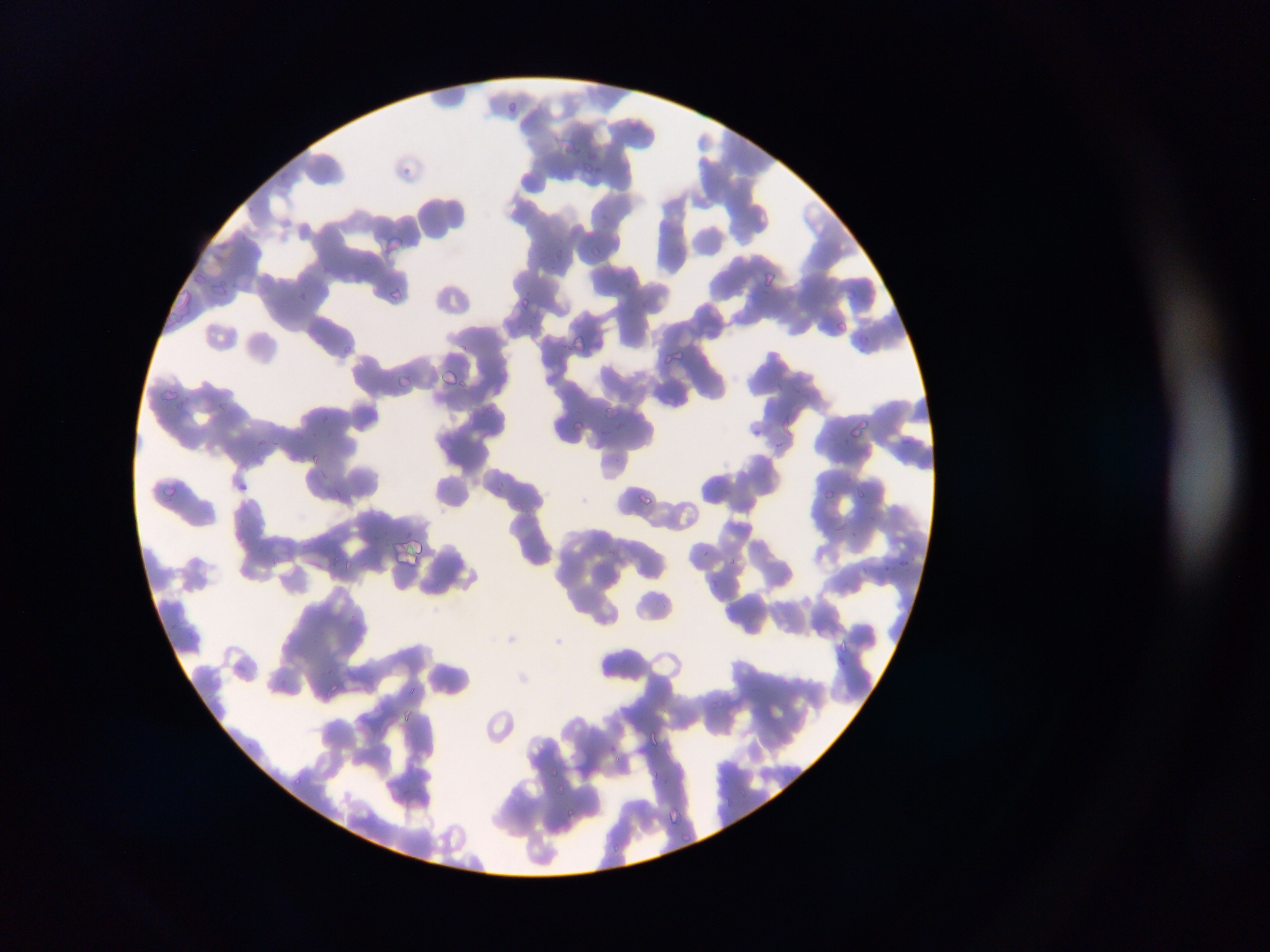

country = Ghana
Plasmodium parasite locations = approximate bounding boxes as (left, top, right, bottom) in pixels: (504, 98, 521, 113), (566, 141, 585, 159), (399, 155, 425, 179), (582, 161, 599, 176), (384, 232, 403, 255), (592, 243, 605, 255), (552, 246, 564, 258), (763, 271, 777, 287), (386, 281, 406, 301), (517, 292, 535, 311), (834, 319, 848, 331), (572, 336, 594, 353), (667, 345, 699, 370), (443, 366, 466, 386), (394, 369, 413, 389), (162, 388, 183, 404), (170, 391, 190, 410), (600, 402, 621, 424), (849, 416, 869, 440), (571, 417, 585, 433), (256, 436, 267, 447), (307, 449, 326, 466), (315, 463, 332, 483), (153, 476, 181, 501), (823, 487, 835, 500), (639, 489, 657, 503), (855, 489, 868, 501), (512, 500, 526, 511), (401, 538, 427, 564), (703, 551, 714, 557), (329, 554, 344, 567), (272, 557, 281, 567), (899, 557, 911, 569), (730, 558, 741, 566), (345, 561, 359, 572), (840, 637, 853, 650), (326, 682, 339, 697), (716, 700, 727, 708), (399, 708, 417, 725), (647, 728, 664, 747), (551, 776, 565, 795), (293, 777, 305, 786), (567, 808, 584, 816), (668, 808, 688, 826), (679, 832, 701, 845), (613, 839, 624, 857)
image size = 1270×952 pixels
field of view = single
capture = mobile-phone photograph through a microscope
preparation = thin blood film